Assess this cell for malaria.
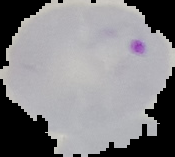

It is parasitized.

Image is 175×157 pixels. The area outside the segmented cell region is set to black. From a thin blood film.